Assess this cell for malaria.
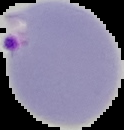
Parasitized.

image_size: 124×130 pixels
preparation: thin blood film
image_type: segmented cell region with the area outside set to black